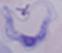
Summary:
  - Identification: trypanosome
  - Modality: photomicrograph
  - Magnification: 1000x